Locate every blood parasite and identify its species.
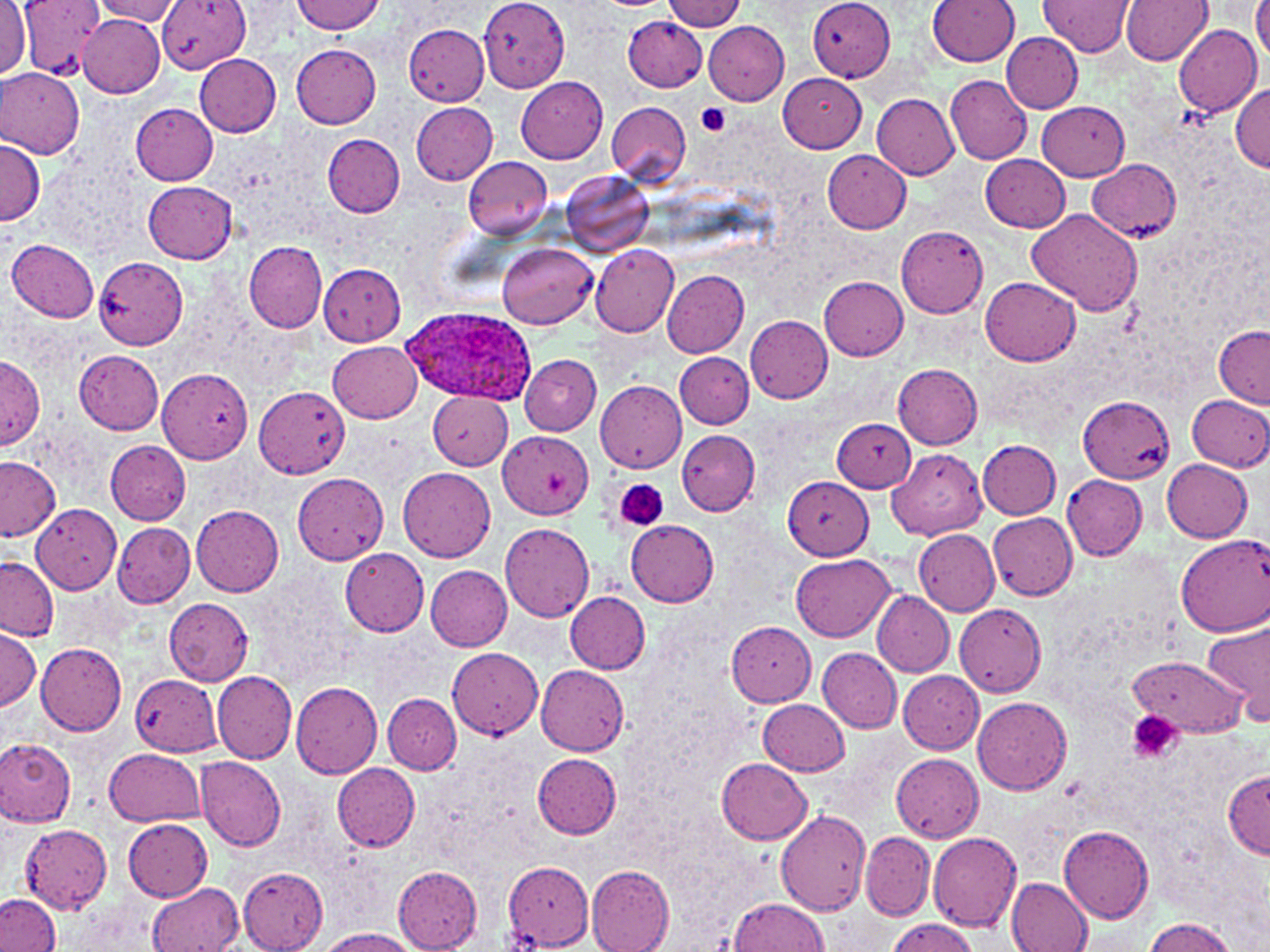
Approximate bounding boxes as named x1/y1/x2/y2 corners in pixels.
Plasmodium ovale-infected red blood cells: (x1=397, y1=309, x2=538, y2=407).
No Plasmodium falciparum, Plasmodium malariae, Plasmodium vivax, Babesia divergens, or Trypanosoma brucei observed.

Summary:
  - Platelet locations: (x1=695, y1=103, x2=733, y2=136), (x1=615, y1=479, x2=669, y2=531), (x1=1128, y1=711, x2=1184, y2=765)
  - Uninfected red blood cell locations: (x1=0, y1=0, x2=30, y2=79), (x1=19, y1=0, x2=104, y2=80), (x1=160, y1=0, x2=250, y2=74), (x1=290, y1=0, x2=385, y2=34), (x1=664, y1=0, x2=746, y2=32), (x1=809, y1=0, x2=896, y2=82), (x1=928, y1=0, x2=1019, y2=65), (x1=1039, y1=0, x2=1134, y2=57), (x1=1120, y1=0, x2=1213, y2=66), (x1=1251, y1=0, x2=1270, y2=58), (x1=92, y1=1, x2=185, y2=24), (x1=481, y1=2, x2=571, y2=97), (x1=622, y1=15, x2=707, y2=92), (x1=78, y1=17, x2=164, y2=99), (x1=703, y1=21, x2=789, y2=105), (x1=1173, y1=24, x2=1261, y2=116), (x1=404, y1=25, x2=490, y2=104), (x1=1002, y1=33, x2=1083, y2=113), (x1=291, y1=44, x2=381, y2=128), (x1=194, y1=54, x2=280, y2=135), (x1=0, y1=67, x2=83, y2=159), (x1=779, y1=72, x2=867, y2=153), (x1=945, y1=75, x2=1033, y2=164), (x1=515, y1=77, x2=608, y2=163), (x1=1232, y1=84, x2=1270, y2=171), (x1=873, y1=93, x2=959, y2=179), (x1=606, y1=101, x2=690, y2=186), (x1=1038, y1=101, x2=1129, y2=180), (x1=131, y1=103, x2=217, y2=184), (x1=411, y1=103, x2=498, y2=184), (x1=322, y1=134, x2=404, y2=217), (x1=1, y1=137, x2=43, y2=227), (x1=821, y1=148, x2=911, y2=232), (x1=980, y1=153, x2=1069, y2=232), (x1=462, y1=156, x2=554, y2=240), (x1=1088, y1=159, x2=1180, y2=240), (x1=562, y1=171, x2=652, y2=257), (x1=143, y1=181, x2=238, y2=262), (x1=1026, y1=208, x2=1144, y2=316), (x1=896, y1=226, x2=988, y2=318), (x1=7, y1=240, x2=99, y2=321), (x1=244, y1=242, x2=328, y2=331), (x1=498, y1=242, x2=597, y2=329), (x1=591, y1=243, x2=680, y2=336), (x1=93, y1=256, x2=187, y2=350), (x1=318, y1=264, x2=405, y2=345), (x1=661, y1=268, x2=749, y2=357), (x1=820, y1=276, x2=908, y2=359), (x1=981, y1=277, x2=1081, y2=366), (x1=746, y1=315, x2=833, y2=402), (x1=1214, y1=326, x2=1270, y2=408), (x1=327, y1=340, x2=421, y2=422), (x1=75, y1=351, x2=165, y2=434), (x1=675, y1=353, x2=753, y2=429), (x1=520, y1=354, x2=601, y2=434), (x1=1, y1=357, x2=43, y2=450), (x1=892, y1=364, x2=983, y2=448), (x1=157, y1=369, x2=252, y2=462), (x1=595, y1=378, x2=686, y2=472), (x1=254, y1=385, x2=351, y2=479), (x1=428, y1=391, x2=514, y2=470), (x1=1188, y1=394, x2=1270, y2=472), (x1=1078, y1=396, x2=1174, y2=482), (x1=832, y1=418, x2=915, y2=493), (x1=676, y1=429, x2=760, y2=516), (x1=500, y1=431, x2=592, y2=520), (x1=105, y1=440, x2=190, y2=524), (x1=979, y1=441, x2=1062, y2=518), (x1=888, y1=449, x2=985, y2=539), (x1=0, y1=456, x2=62, y2=543), (x1=1161, y1=458, x2=1253, y2=543), (x1=398, y1=467, x2=496, y2=562), (x1=293, y1=473, x2=388, y2=563), (x1=784, y1=475, x2=874, y2=559), (x1=1062, y1=475, x2=1148, y2=559), (x1=30, y1=503, x2=121, y2=593), (x1=189, y1=504, x2=285, y2=596), (x1=988, y1=513, x2=1077, y2=601), (x1=625, y1=520, x2=719, y2=607), (x1=113, y1=522, x2=194, y2=607), (x1=500, y1=523, x2=594, y2=623), (x1=914, y1=529, x2=1000, y2=614), (x1=1175, y1=533, x2=1270, y2=634), (x1=341, y1=549, x2=430, y2=637), (x1=793, y1=554, x2=895, y2=641), (x1=0, y1=555, x2=58, y2=641), (x1=425, y1=566, x2=513, y2=651), (x1=564, y1=590, x2=651, y2=674), (x1=872, y1=590, x2=955, y2=676), (x1=163, y1=598, x2=253, y2=684), (x1=956, y1=604, x2=1044, y2=696), (x1=1203, y1=618, x2=1270, y2=726), (x1=726, y1=622, x2=816, y2=706), (x1=0, y1=628, x2=40, y2=713), (x1=36, y1=643, x2=127, y2=735), (x1=448, y1=647, x2=543, y2=739), (x1=818, y1=648, x2=903, y2=733), (x1=1129, y1=656, x2=1245, y2=737), (x1=536, y1=664, x2=629, y2=755), (x1=130, y1=672, x2=223, y2=757), (x1=213, y1=672, x2=297, y2=765), (x1=899, y1=672, x2=984, y2=753), (x1=291, y1=681, x2=382, y2=778), (x1=383, y1=694, x2=461, y2=773), (x1=973, y1=695, x2=1071, y2=794), (x1=758, y1=700, x2=850, y2=775), (x1=0, y1=739, x2=76, y2=827), (x1=105, y1=748, x2=204, y2=826), (x1=533, y1=753, x2=622, y2=838), (x1=890, y1=753, x2=984, y2=841), (x1=196, y1=756, x2=287, y2=850), (x1=716, y1=759, x2=813, y2=845), (x1=332, y1=761, x2=421, y2=852), (x1=1222, y1=768, x2=1270, y2=860), (x1=776, y1=808, x2=873, y2=917), (x1=122, y1=818, x2=213, y2=901), (x1=21, y1=823, x2=113, y2=912), (x1=1060, y1=826, x2=1155, y2=923), (x1=927, y1=831, x2=1022, y2=931), (x1=860, y1=832, x2=935, y2=921), (x1=502, y1=862, x2=594, y2=949), (x1=238, y1=865, x2=329, y2=951), (x1=586, y1=866, x2=675, y2=952), (x1=393, y1=867, x2=484, y2=951), (x1=1006, y1=876, x2=1094, y2=952), (x1=148, y1=883, x2=245, y2=951), (x1=0, y1=894, x2=61, y2=951), (x1=728, y1=897, x2=830, y2=951), (x1=1142, y1=917, x2=1235, y2=951), (x1=886, y1=918, x2=977, y2=952), (x1=318, y1=927, x2=420, y2=952)
  - Slide-level diagnosis: Plasmodium ovale
  - Magnification: 1000x
  - Field of view: single
  - Modality: optical microscopy
  - Preparation: thin blood smear
  - Image size: 1270×952 pixels
  - Stain: May-Grünwald-Giemsa